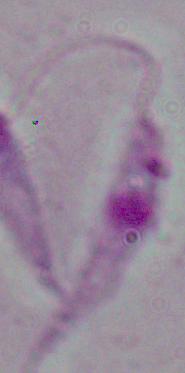
Summary:
  - Modality: photomicrograph
  - Magnification: 1000x
  - Identification: Leishmania